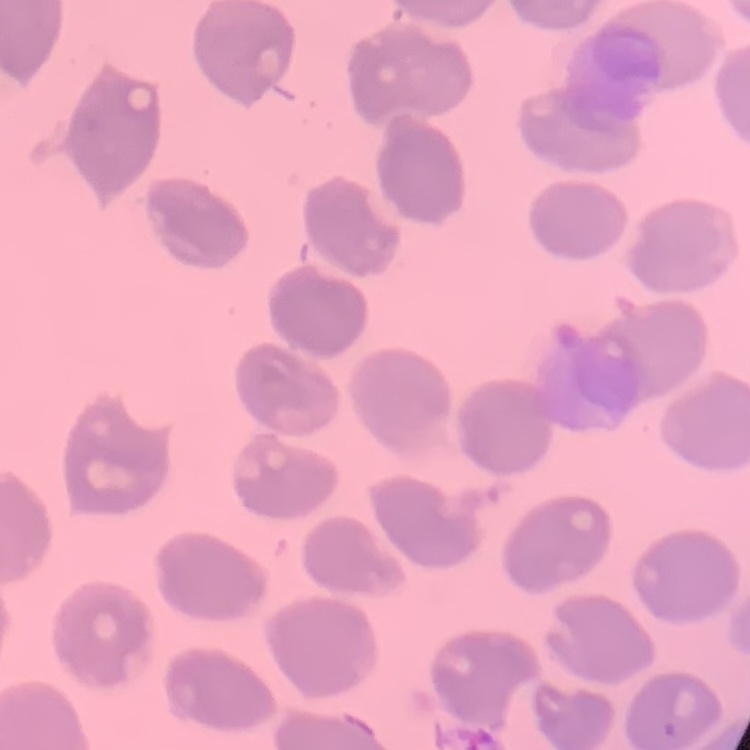

The red blood cells exhibit no rouleaux formation. Stained with either Field's or Giemsa. One tile cut from a larger photomicrograph. Thin blood smear.